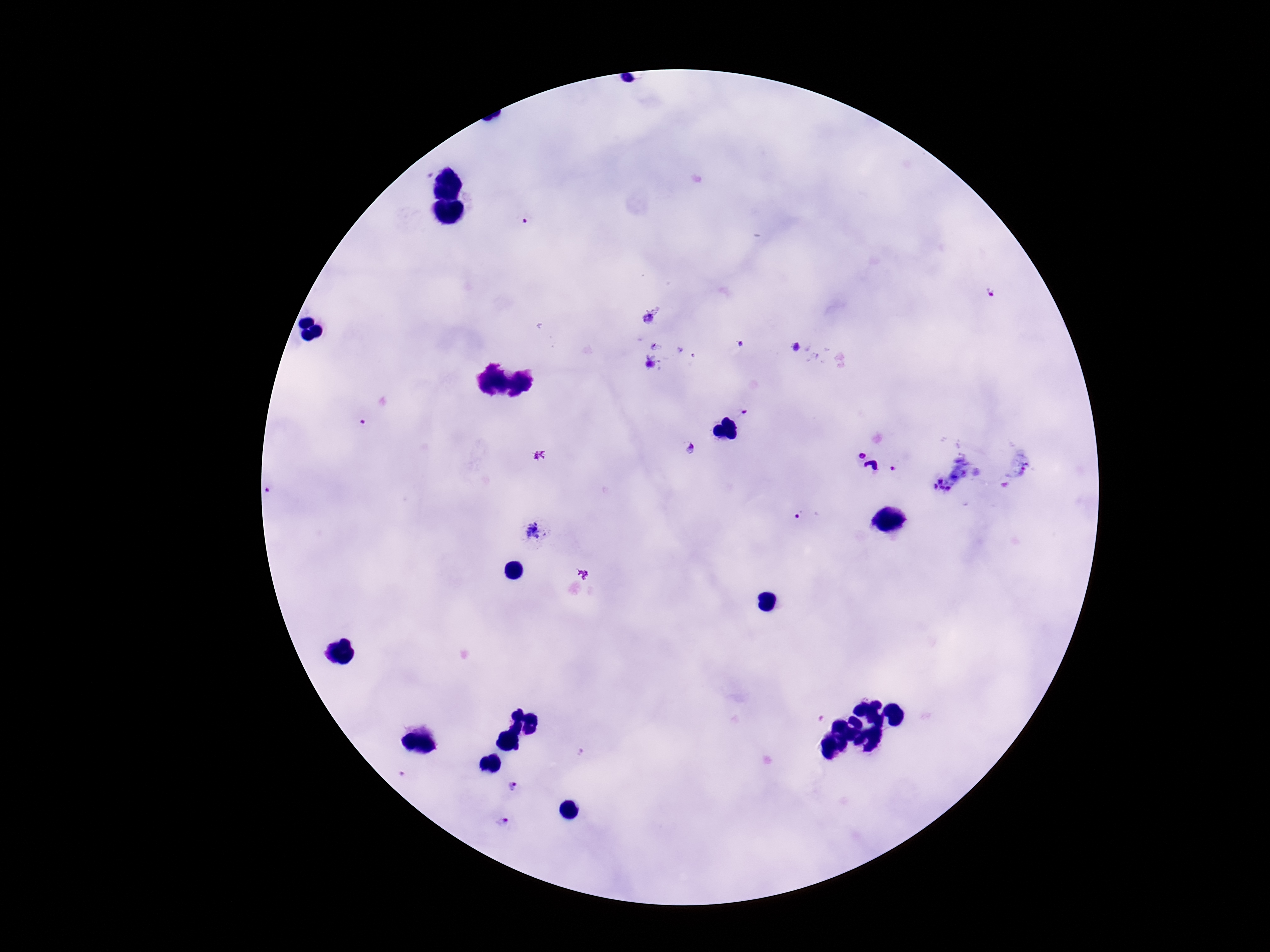
Approximate object centers, in pixels from the top-left corner.
Summary:
  - Plasmodium parasite locations: (x=523, y=223), (x=989, y=293), (x=649, y=321), (x=741, y=343), (x=796, y=347), (x=650, y=364), (x=745, y=409), (x=365, y=422), (x=691, y=448), (x=861, y=452), (x=943, y=485), (x=272, y=490), (x=798, y=516), (x=532, y=530), (x=512, y=785), (x=502, y=821)
  - Field of view: one from this slide
  - Stain: Giemsa
  - Preparation: thick blood smear
  - Image size: 1270×952 pixels
  - Capture: smartphone camera through the microscope eyepiece
  - Patient malaria status: infected
  - Magnification: 100x